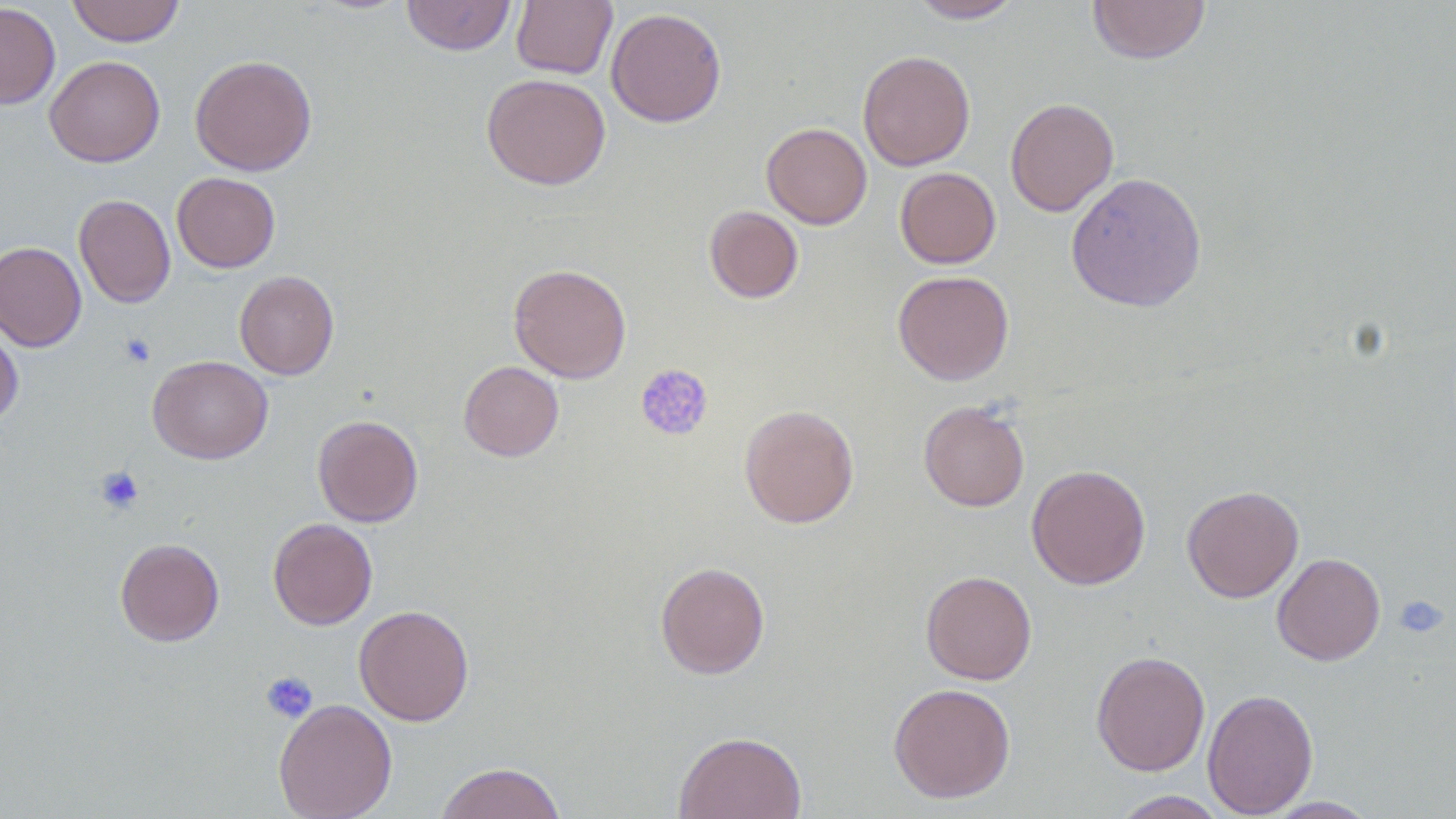

{
  "slide_level_diagnosis": "negative for blood parasites",
  "platelet_locations": "approximate bounding boxes as [x1, y1, x2, y2] in pixels: [119, 333, 156, 368], [635, 364, 714, 443], [94, 466, 144, 515], [1393, 595, 1449, 638], [260, 671, 318, 724]",
  "preparation": "thin blood smear",
  "magnification": "1000x",
  "uninfected_red_blood_cell_locations": "approximate bounding boxes as [x1, y1, x2, y2] in pixels: [66, 0, 184, 47], [401, 0, 516, 56], [511, 0, 617, 79], [910, 0, 1026, 23], [1086, 1, 1212, 64], [0, 2, 61, 109], [606, 7, 727, 127], [857, 50, 976, 171], [190, 54, 317, 176], [44, 56, 165, 167], [481, 72, 611, 190], [1005, 97, 1119, 216], [761, 123, 872, 229], [895, 167, 1001, 269], [1066, 171, 1207, 312], [172, 172, 280, 273], [74, 194, 175, 308], [704, 206, 804, 304], [0, 241, 86, 351], [508, 263, 632, 383], [892, 269, 1014, 385], [234, 270, 339, 380], [0, 322, 23, 428], [148, 355, 273, 463], [458, 361, 564, 461], [918, 400, 1030, 512], [739, 405, 859, 528], [312, 414, 424, 527], [1026, 464, 1151, 590], [1182, 485, 1304, 602], [268, 518, 377, 630], [115, 537, 224, 646], [1272, 552, 1385, 665], [655, 561, 770, 679], [921, 570, 1037, 685], [353, 605, 474, 726], [1091, 650, 1211, 776], [888, 682, 1016, 803], [1203, 688, 1318, 818], [273, 698, 398, 819], [673, 730, 807, 819], [434, 761, 567, 819], [1110, 790, 1230, 818], [1261, 796, 1380, 818]",
  "modality": "light microscopy",
  "image_size": "1456×819 pixels",
  "field_of_view": "one of a larger specimen"
}